Report the malaria status of this cell.
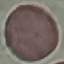
It is uninfected.

capture = smartphone camera at the microscope eyepiece
preparation = thin blood film
image type = cell patch, automatically extracted from a larger field of view and resized to 64 × 64 pixels
stain = Giemsa